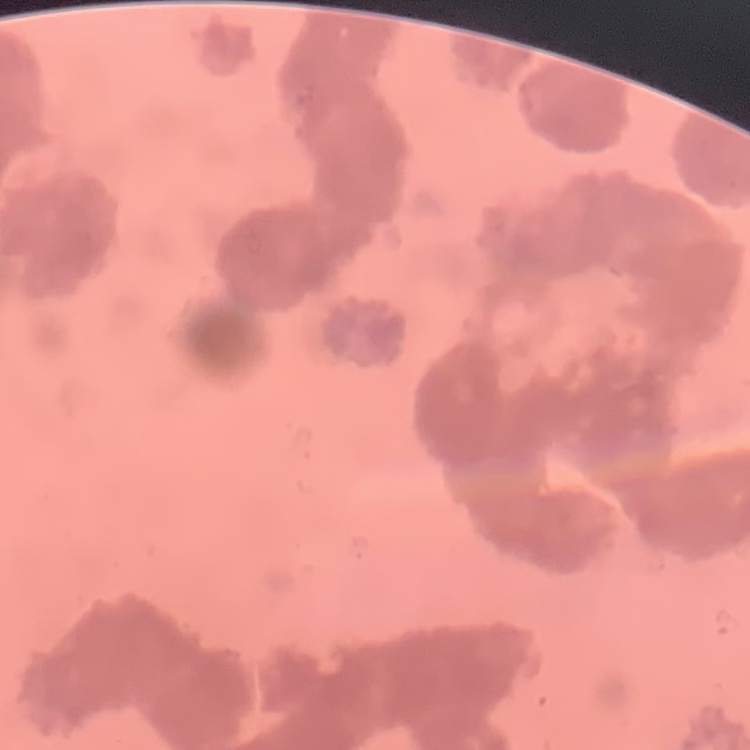
erythrocyte_morphology: rouleaux formation
stain: Field's or Giemsa
preparation: thin peripheral smear
image_type: one tile cut from a larger photomicrograph